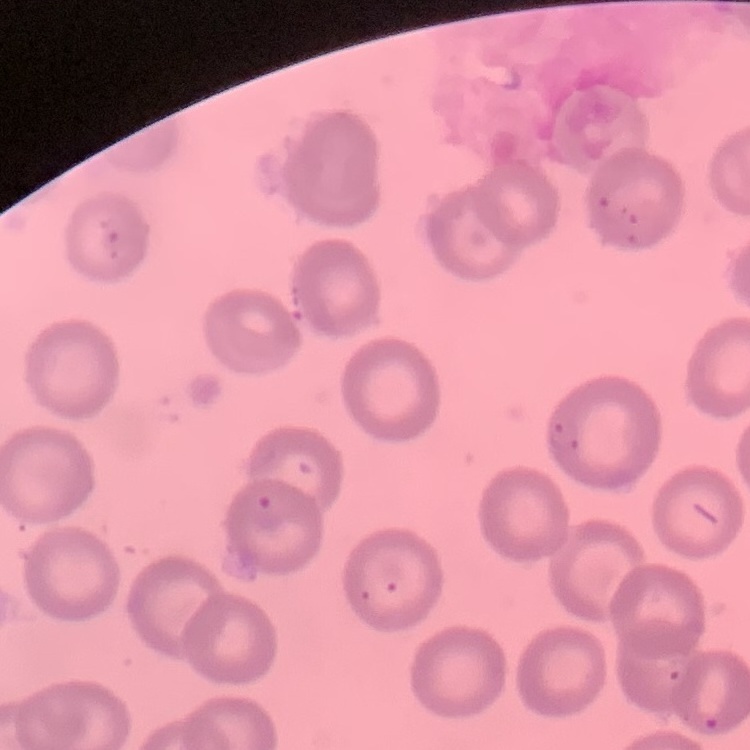

Summary:
  - Erythrocyte morphology: no rouleaux formation
  - Stain: Field's or Giemsa
  - Image type: one tile cut from a larger photomicrograph
  - Preparation: thin blood film